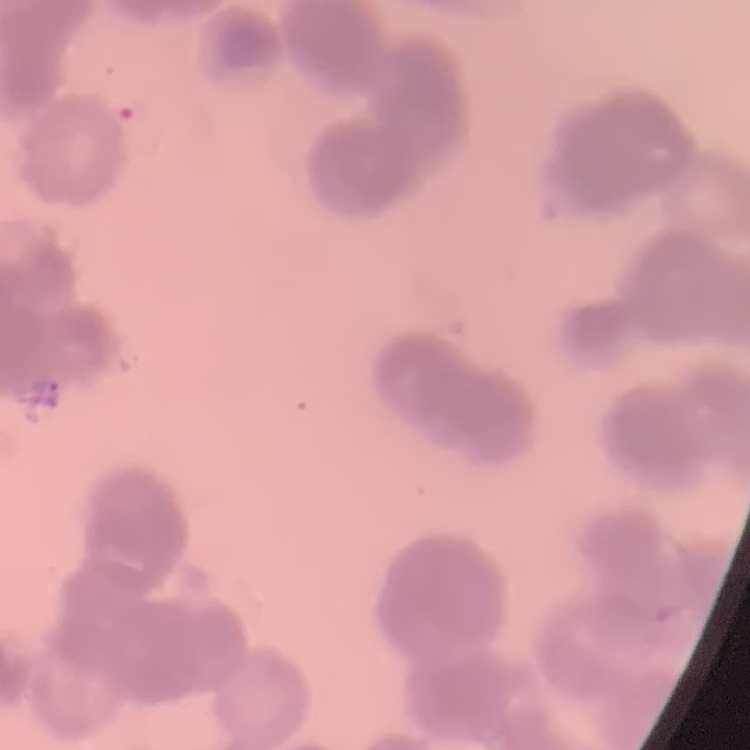

The erythrocytes show rouleaux formation. One tile cut from a larger photomicrograph. Stained with either Field's or Giemsa. Thin blood film.